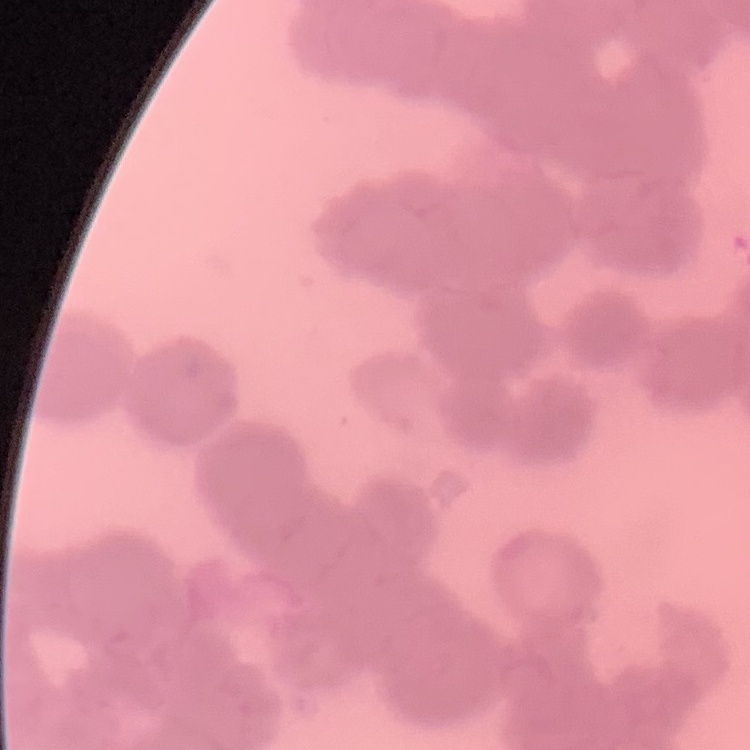 The red blood cells show rouleaux formation. Stained with either Field's or Giemsa. One tile cut from a larger photomicrograph. Thin blood smear.